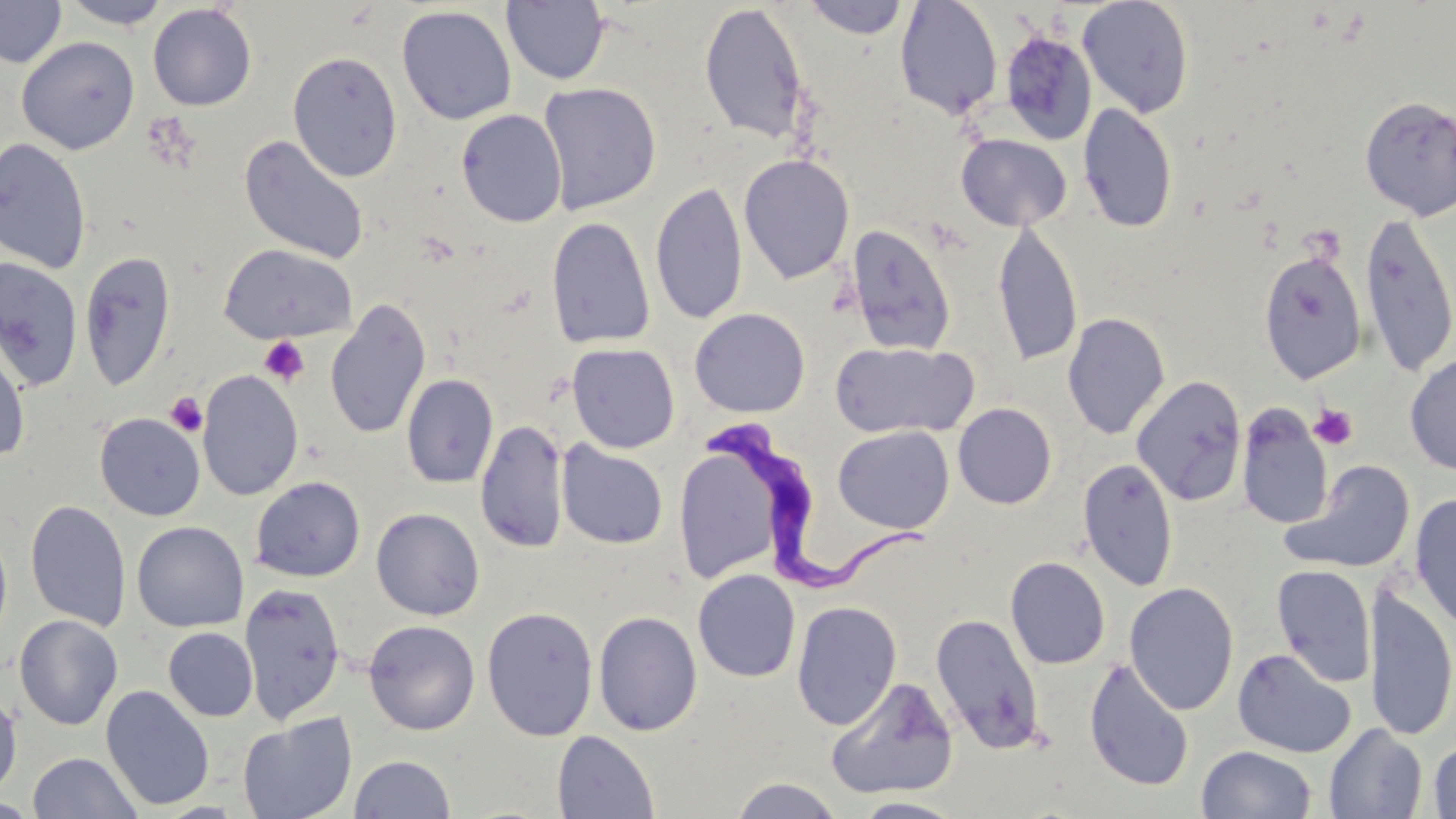
Summary:
  - Coordinate format: approximate bounding boxes as (x1, y1, x2, y2) in pixels
  - Platelet locations: (260, 336, 308, 386), (165, 392, 208, 437), (1309, 403, 1358, 450)
  - Uninfected red blood cell locations: (501, 0, 609, 86), (802, 0, 910, 39), (894, 0, 1004, 120), (1077, 0, 1194, 118), (0, 1, 66, 68), (59, 1, 172, 29), (147, 3, 257, 111), (698, 3, 812, 146), (396, 6, 517, 125), (1000, 31, 1097, 145), (16, 36, 140, 154), (288, 51, 402, 181), (538, 82, 662, 215), (1359, 97, 1456, 220), (1078, 103, 1178, 233), (456, 109, 567, 227), (956, 134, 1071, 231), (239, 135, 369, 266), (0, 137, 92, 274), (738, 154, 855, 284), (650, 180, 748, 326), (1359, 213, 1456, 376), (546, 216, 655, 349), (992, 220, 1084, 367), (845, 224, 957, 356), (219, 244, 357, 345), (79, 250, 177, 392), (1258, 251, 1367, 384), (0, 258, 83, 392), (325, 300, 432, 439), (689, 308, 810, 418), (1062, 312, 1170, 440), (0, 337, 32, 465), (829, 341, 978, 439), (567, 343, 680, 453), (1404, 352, 1456, 475), (197, 370, 304, 501), (401, 374, 498, 489), (1132, 375, 1247, 506), (953, 403, 1057, 509), (1236, 405, 1333, 529), (94, 412, 205, 521), (475, 419, 569, 553), (832, 425, 954, 534), (556, 441, 669, 549), (673, 443, 785, 584), (1078, 458, 1178, 592), (1283, 460, 1417, 574), (250, 476, 365, 582), (1408, 492, 1456, 632), (25, 499, 131, 632), (371, 507, 485, 620), (132, 521, 249, 633), (0, 523, 13, 652), (1005, 556, 1110, 669), (1272, 564, 1377, 687), (692, 569, 800, 682), (239, 582, 346, 724), (1124, 582, 1239, 715), (1364, 586, 1456, 742), (791, 600, 902, 730), (481, 606, 599, 741), (593, 610, 703, 736), (930, 613, 1045, 755), (14, 614, 123, 731), (363, 619, 480, 735), (163, 627, 258, 721), (1232, 648, 1356, 758), (1084, 659, 1195, 791), (826, 677, 959, 799), (100, 685, 215, 811), (0, 692, 22, 800), (237, 713, 357, 819), (1324, 723, 1427, 818), (552, 730, 660, 819), (1428, 738, 1456, 818), (1197, 745, 1317, 818), (28, 752, 142, 819), (349, 754, 455, 818), (729, 776, 845, 818), (852, 797, 966, 818)
  - Trypanosoma brucei locations: (706, 417, 949, 600)
  - Slide-level diagnosis: Trypanosoma brucei
  - Preparation: thin blood film
  - Field of view: single
  - Image size: 1456×819 pixels
  - Stain: May-Grünwald-Giemsa
  - Magnification: 1000x
  - Modality: optical microscopy